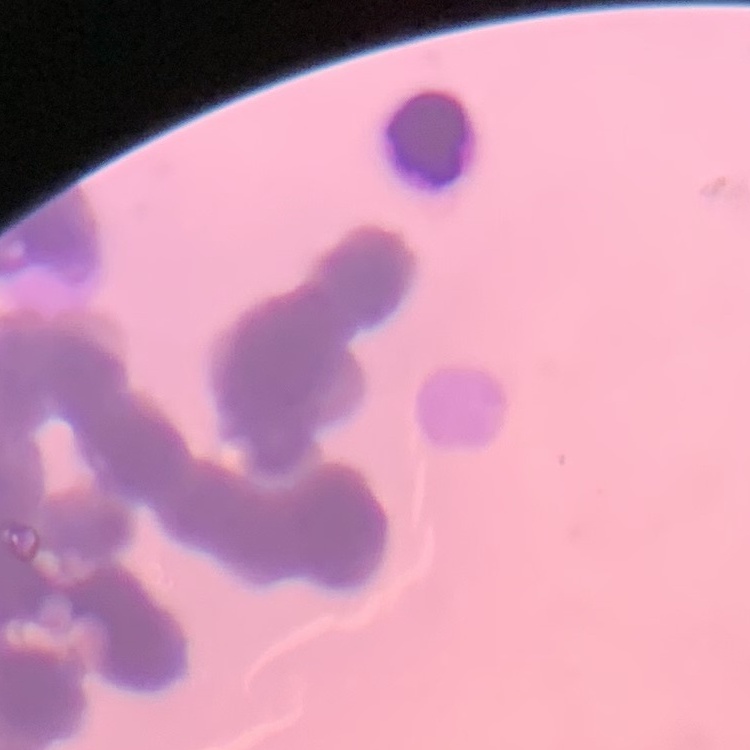 The red blood cells show rouleaux formation. Thin blood film. Field's or Giemsa stain. Square crop of a larger photomicrograph.